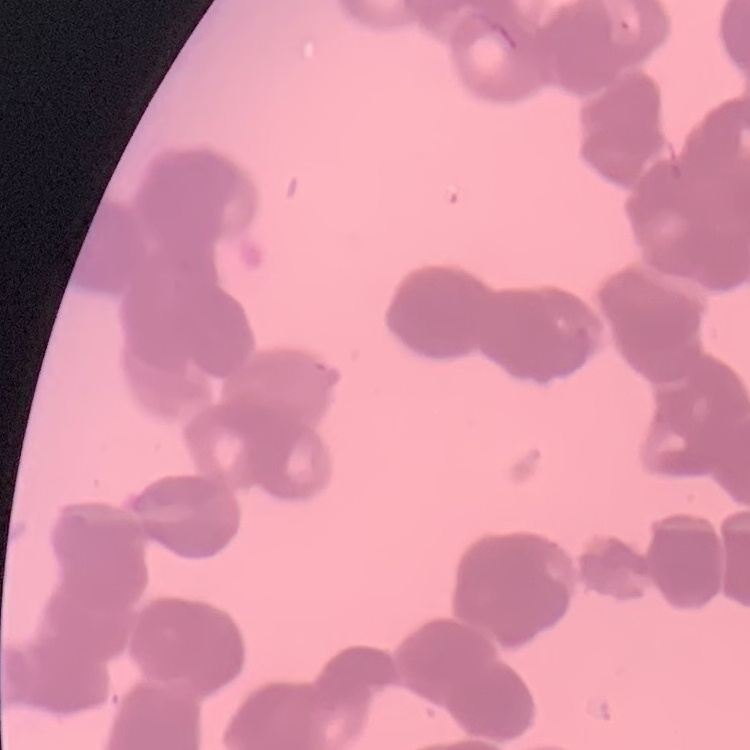

erythrocyte_morphology: rouleaux formation
image_type: one tile cut from a larger photomicrograph
preparation: thin blood smear
stain: Field's or Giemsa